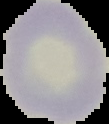

malaria_status: uninfected
image_type: segmented cell region with the area outside set to black
image_size: 109×124 pixels
preparation: thin blood film